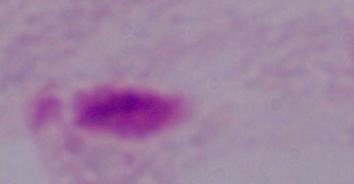
A trichomonad is seen. Photomicrograph. 1000x magnification.